Give the extent of all uninfected red blood cells.
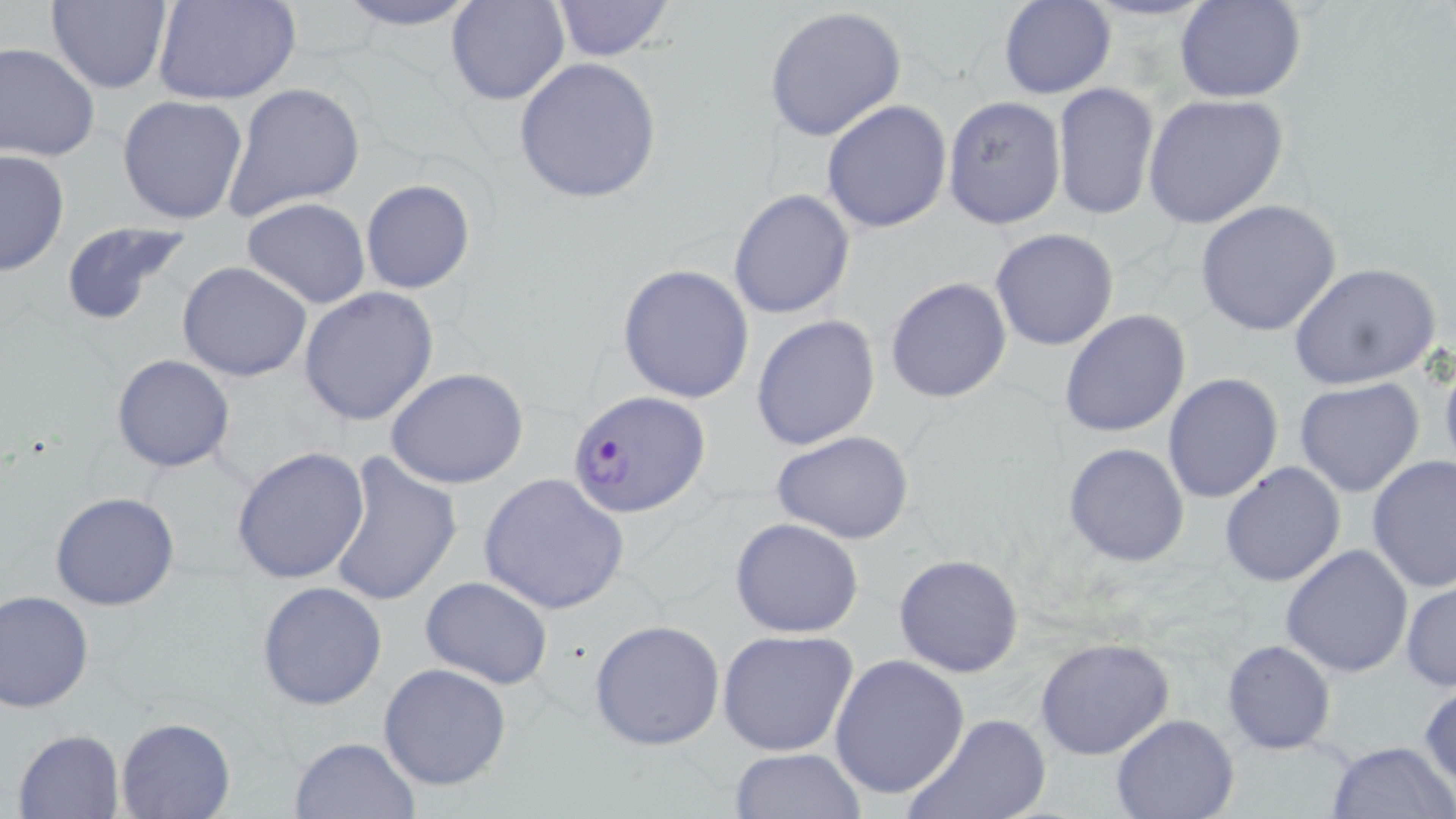

Approximate bounding boxes as named x1/y1/x2/y2 corners in pixels.
Uninfected red blood cells: (x1=155, y1=0, x2=301, y2=106), (x1=329, y1=0, x2=485, y2=32), (x1=446, y1=0, x2=567, y2=106), (x1=550, y1=0, x2=677, y2=61), (x1=998, y1=0, x2=1115, y2=99), (x1=1176, y1=0, x2=1306, y2=103), (x1=46, y1=2, x2=171, y2=91), (x1=765, y1=6, x2=908, y2=143), (x1=1, y1=41, x2=101, y2=163), (x1=512, y1=58, x2=664, y2=204), (x1=221, y1=83, x2=365, y2=223), (x1=1052, y1=83, x2=1160, y2=220), (x1=1142, y1=93, x2=1289, y2=229), (x1=116, y1=95, x2=249, y2=226), (x1=942, y1=95, x2=1066, y2=230), (x1=821, y1=99, x2=952, y2=234), (x1=0, y1=150, x2=70, y2=277), (x1=360, y1=178, x2=477, y2=295), (x1=728, y1=189, x2=856, y2=319), (x1=242, y1=198, x2=371, y2=308), (x1=1195, y1=200, x2=1342, y2=337), (x1=60, y1=221, x2=193, y2=330), (x1=990, y1=228, x2=1120, y2=351), (x1=176, y1=261, x2=313, y2=383), (x1=616, y1=263, x2=756, y2=404), (x1=1290, y1=263, x2=1443, y2=393), (x1=885, y1=277, x2=1012, y2=404), (x1=298, y1=287, x2=440, y2=426), (x1=1059, y1=309, x2=1190, y2=438), (x1=752, y1=314, x2=880, y2=450), (x1=1438, y1=348, x2=1456, y2=486), (x1=113, y1=354, x2=235, y2=474), (x1=386, y1=366, x2=530, y2=489), (x1=1163, y1=373, x2=1284, y2=505), (x1=1295, y1=378, x2=1425, y2=497), (x1=771, y1=429, x2=917, y2=544), (x1=1064, y1=442, x2=1190, y2=567), (x1=231, y1=445, x2=372, y2=583), (x1=327, y1=452, x2=463, y2=607), (x1=1366, y1=456, x2=1456, y2=594), (x1=1220, y1=461, x2=1346, y2=588), (x1=479, y1=471, x2=630, y2=615), (x1=50, y1=491, x2=180, y2=609), (x1=730, y1=517, x2=864, y2=638), (x1=1280, y1=544, x2=1414, y2=679), (x1=893, y1=554, x2=1024, y2=676), (x1=420, y1=577, x2=552, y2=689), (x1=1401, y1=579, x2=1456, y2=691), (x1=257, y1=581, x2=388, y2=709), (x1=0, y1=589, x2=96, y2=713), (x1=589, y1=619, x2=725, y2=750), (x1=716, y1=630, x2=861, y2=758), (x1=1034, y1=637, x2=1175, y2=760), (x1=1222, y1=639, x2=1336, y2=754), (x1=827, y1=654, x2=970, y2=800), (x1=378, y1=662, x2=513, y2=792), (x1=1417, y1=685, x2=1455, y2=794), (x1=902, y1=711, x2=1052, y2=819), (x1=1111, y1=712, x2=1239, y2=818), (x1=115, y1=717, x2=235, y2=819), (x1=12, y1=729, x2=124, y2=819), (x1=287, y1=735, x2=419, y2=818), (x1=1324, y1=739, x2=1455, y2=819), (x1=727, y1=748, x2=866, y2=819).

Plasmodium falciparum-infected red blood cell locations: (x1=567, y1=390, x2=709, y2=517). Slide-level diagnosis: Plasmodium falciparum. Image is 1456×819 pixels. Light microscopy. Captured at 1000x magnification. May-Grünwald-Giemsa-stained preparation. Single field of view. Thin blood smear.